Comment on the morphology of the erythrocytes.
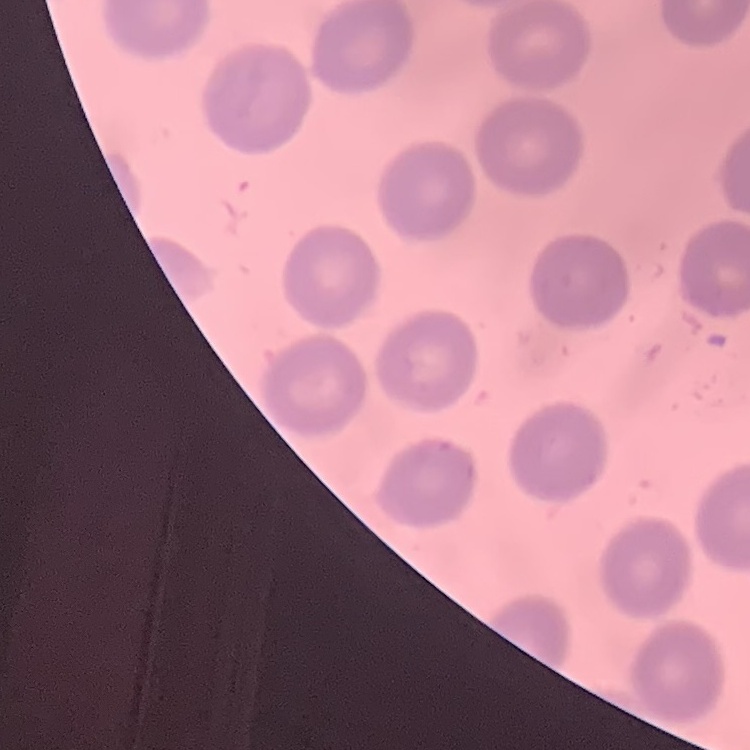
They show no rouleaux formation.

Summary:
  - Stain: Field's or Giemsa
  - Preparation: thin blood smear
  - Image type: square crop of a larger photomicrograph